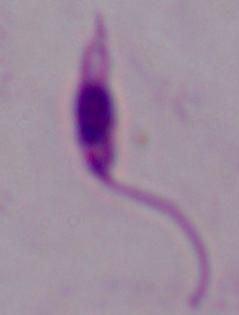 Photomicrograph. Captured at 1000x magnification. A Leishmania parasite is seen.